Point out leukocytes.
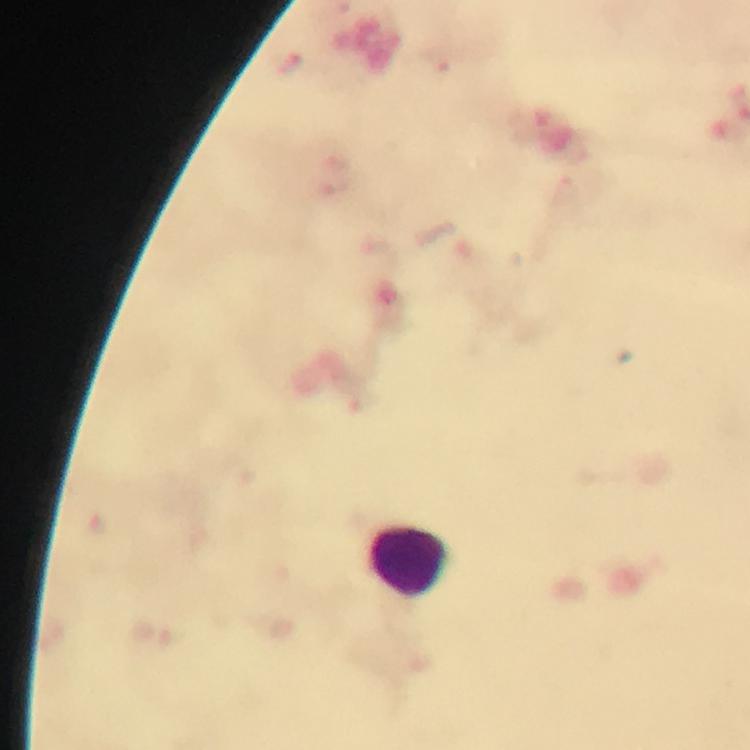
Approximate centers as (x, y) in pixels.
Leukocytes: (409, 561).

Summary:
  - Capture: smartphone mounted on the microscope
  - Stain: Giemsa
  - Image size: 750×750 pixels
  - Context: from a diagnostic examination for malaria
  - Magnification: 100x
  - Immersion oil: used
  - Malaria parasites: none seen
  - Cropped from: one field of view
  - Preparation: thick smear